Locate and identify every blood parasite.
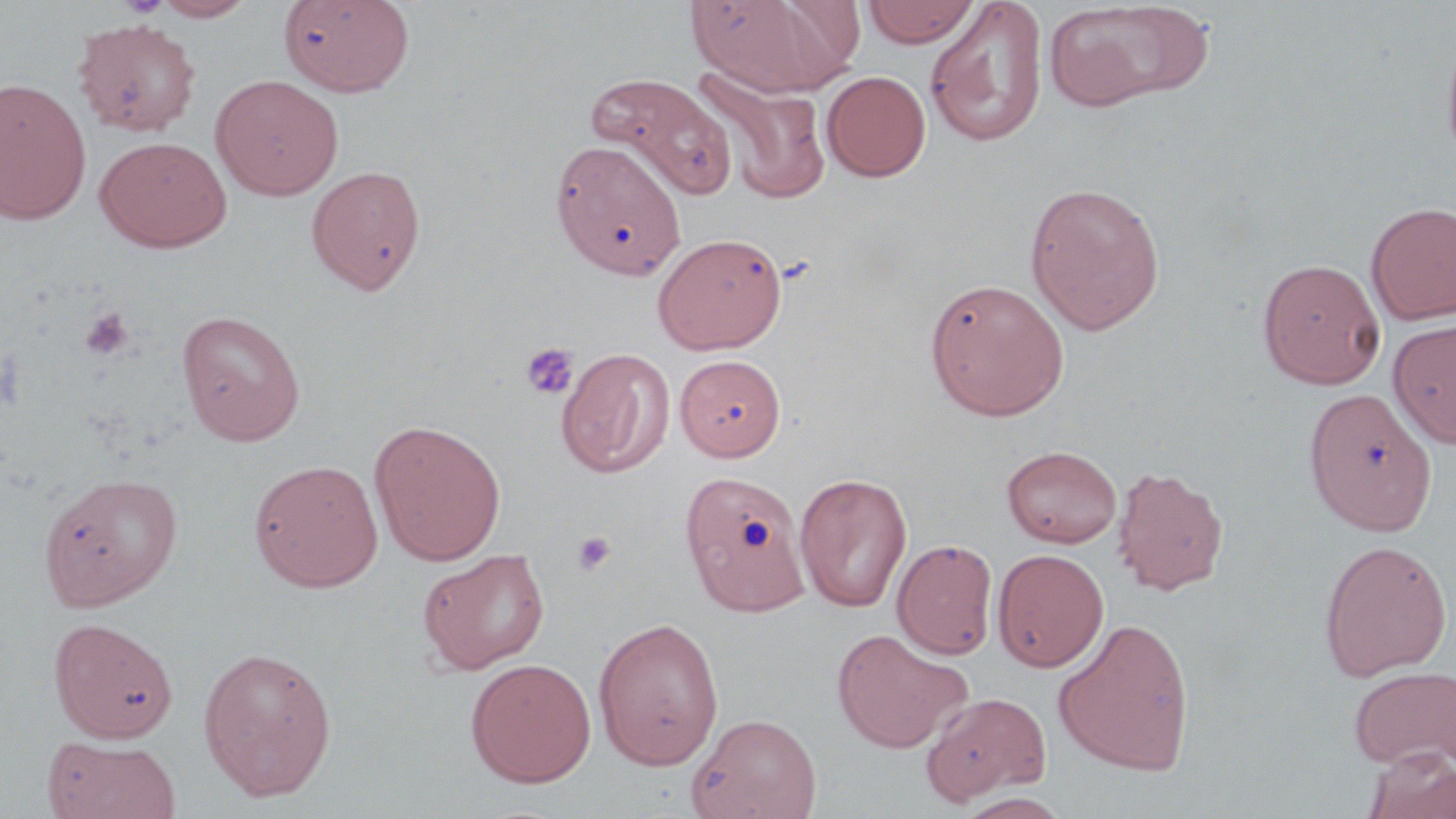
No blood parasites observed.

Approximate bounding boxes as (x1,y1)-(x2,y2) corner pairs in pixels. Platelet locations: (79,307)-(135,362), (520,342)-(579,400), (573,531)-(616,575). Uninfected red blood cell locations: (151,0)-(257,21), (686,0)-(848,97), (862,0)-(981,48), (278,1)-(415,96), (924,1)-(1049,149), (1044,2)-(1208,111), (73,19)-(201,137), (1440,27)-(1456,177), (695,69)-(832,205), (822,71)-(931,182), (587,73)-(738,197), (210,74)-(344,200), (0,78)-(92,225), (95,136)-(232,252), (551,139)-(686,279), (306,165)-(427,294), (1025,182)-(1165,334), (1366,201)-(1456,325), (652,232)-(787,354), (1257,258)-(1386,389), (924,278)-(1069,421), (176,309)-(306,445), (1388,318)-(1456,449), (556,348)-(674,478), (675,355)-(786,461), (1303,388)-(1436,535), (368,419)-(506,565), (1001,445)-(1122,548), (249,459)-(384,592), (1111,465)-(1229,596), (679,470)-(810,616), (38,471)-(183,611), (794,472)-(912,613), (892,539)-(998,659), (1318,539)-(1453,682), (417,547)-(550,675), (992,548)-(1109,672), (592,617)-(724,770), (1053,617)-(1196,776), (48,618)-(178,743), (832,628)-(971,753), (197,645)-(338,801), (464,657)-(596,787), (1348,664)-(1455,770), (921,692)-(1050,804), (688,713)-(822,819), (43,736)-(182,819), (1363,749)-(1456,819), (954,792)-(1073,819). Slide-level diagnosis: negative for blood parasites. Single field of view. May-Grünwald-Giemsa-stained preparation. Captured at 1000x magnification. Image is 1456×819 pixels. Light microscopy. Thin blood film.